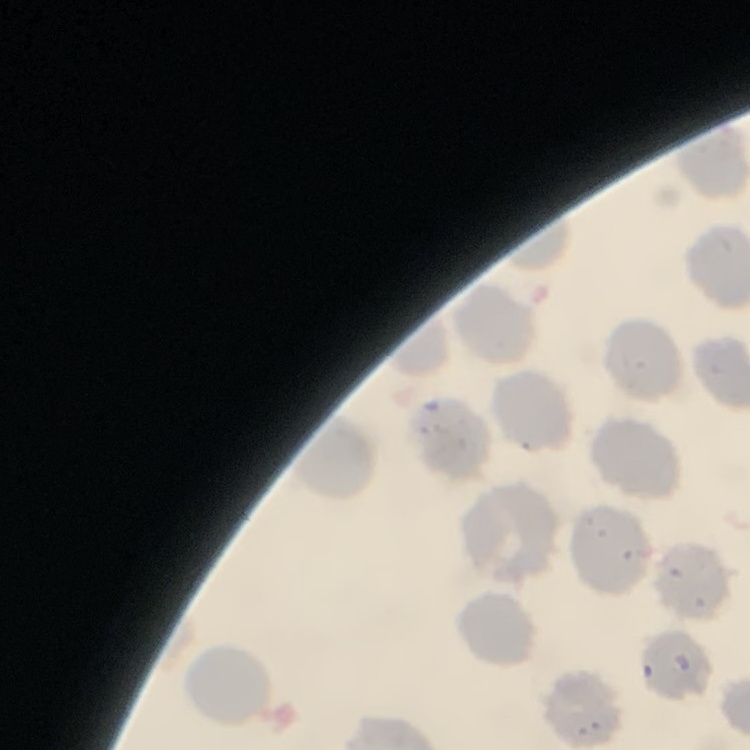
Summary:
  - Erythrocyte morphology: no rouleaux formation
  - Image type: square crop of a larger photomicrograph
  - Preparation: thin blood film
  - Stain: Field's or Giemsa